Outline each Plasmodium falciparum-infected red blood cell.
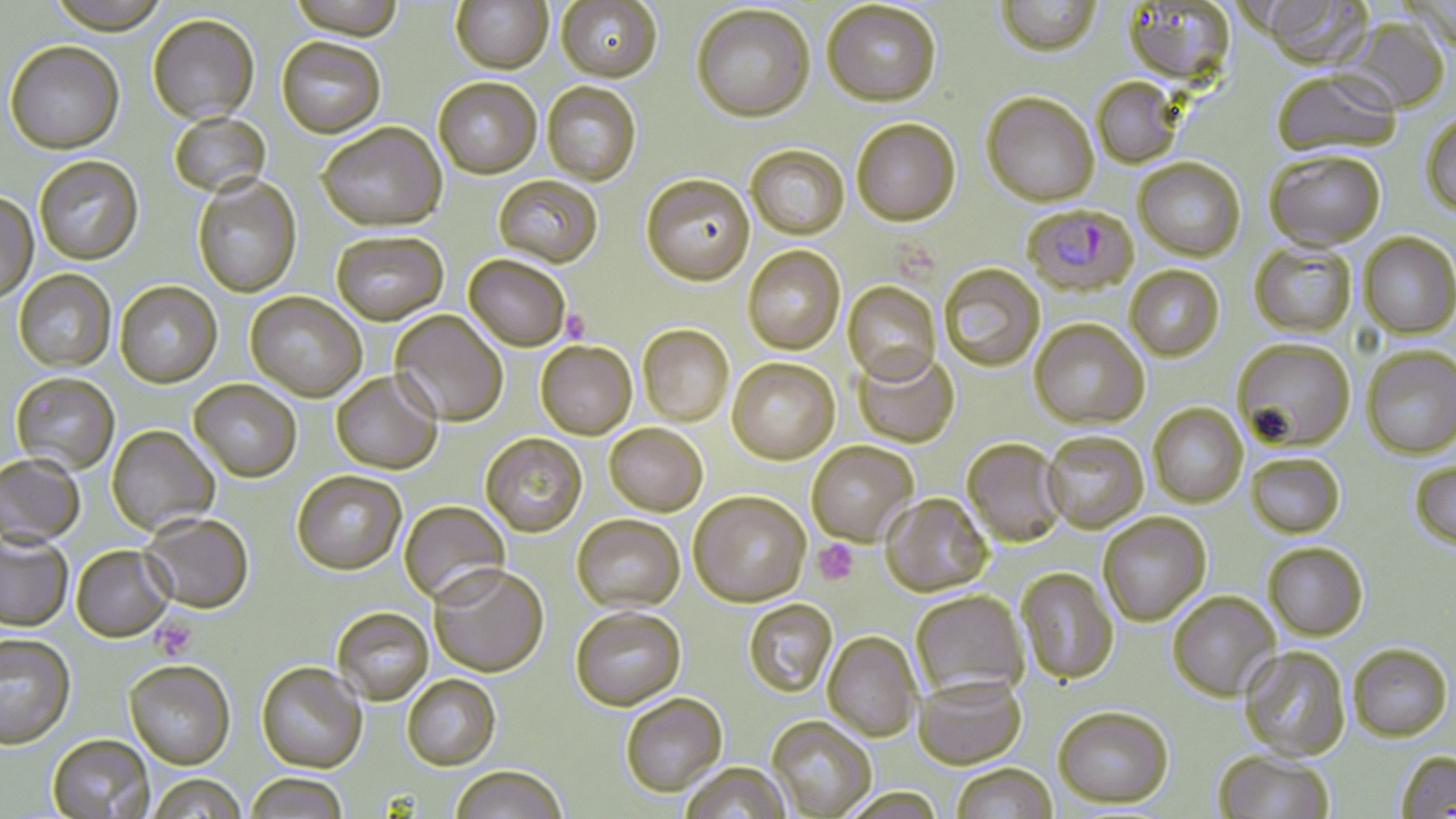

Approximate bounding boxes as named x1/y1/x2/y2 corners in pixels.
Plasmodium falciparum-infected red blood cells: (x1=1025, y1=207, x2=1141, y2=300).

{
  "slide_level_diagnosis": "Plasmodium falciparum",
  "modality": "optical microscopy",
  "field_of_view": "one of a larger specimen",
  "uninfected_red_blood_cell_locations": "approximate bounding boxes as named x1/y1/x2/y2 corners in pixels: (x1=47, y1=0, x2=170, y2=34), (x1=288, y1=0, x2=405, y2=40), (x1=450, y1=0, x2=553, y2=73), (x1=556, y1=0, x2=662, y2=82), (x1=995, y1=0, x2=1102, y2=57), (x1=1258, y1=0, x2=1373, y2=69), (x1=822, y1=1, x2=941, y2=107), (x1=1123, y1=2, x2=1237, y2=87), (x1=692, y1=5, x2=815, y2=123), (x1=148, y1=14, x2=259, y2=123), (x1=1337, y1=17, x2=1451, y2=115), (x1=277, y1=37, x2=386, y2=138), (x1=5, y1=41, x2=124, y2=153), (x1=1271, y1=71, x2=1401, y2=157), (x1=1091, y1=77, x2=1183, y2=170), (x1=433, y1=78, x2=541, y2=178), (x1=542, y1=82, x2=641, y2=185), (x1=981, y1=92, x2=1099, y2=206), (x1=169, y1=112, x2=271, y2=198), (x1=1421, y1=112, x2=1456, y2=219), (x1=851, y1=118, x2=961, y2=226), (x1=317, y1=122, x2=446, y2=231), (x1=746, y1=145, x2=850, y2=239), (x1=1264, y1=150, x2=1385, y2=249), (x1=34, y1=156, x2=143, y2=264), (x1=1133, y1=157, x2=1246, y2=261), (x1=641, y1=173, x2=755, y2=286), (x1=494, y1=175, x2=603, y2=268), (x1=193, y1=176, x2=302, y2=297), (x1=0, y1=192, x2=39, y2=303), (x1=332, y1=231, x2=448, y2=324), (x1=1359, y1=232, x2=1456, y2=339), (x1=1249, y1=242, x2=1356, y2=338), (x1=742, y1=245, x2=845, y2=354), (x1=464, y1=255, x2=571, y2=351), (x1=939, y1=264, x2=1045, y2=372), (x1=1124, y1=265, x2=1224, y2=361), (x1=14, y1=269, x2=116, y2=372), (x1=115, y1=281, x2=222, y2=387), (x1=843, y1=281, x2=941, y2=385), (x1=246, y1=291, x2=366, y2=401), (x1=390, y1=311, x2=509, y2=426), (x1=1029, y1=318, x2=1149, y2=429), (x1=637, y1=324, x2=734, y2=426), (x1=1232, y1=338, x2=1355, y2=451), (x1=536, y1=341, x2=637, y2=439), (x1=1362, y1=346, x2=1456, y2=459), (x1=853, y1=351, x2=960, y2=447), (x1=727, y1=358, x2=839, y2=464), (x1=332, y1=371, x2=443, y2=474), (x1=11, y1=372, x2=120, y2=474), (x1=190, y1=380, x2=302, y2=481), (x1=1148, y1=403, x2=1247, y2=507), (x1=605, y1=423, x2=708, y2=516), (x1=107, y1=425, x2=220, y2=535), (x1=1043, y1=431, x2=1148, y2=533), (x1=480, y1=433, x2=587, y2=536), (x1=961, y1=438, x2=1068, y2=547), (x1=806, y1=440, x2=919, y2=546), (x1=0, y1=453, x2=85, y2=547), (x1=1246, y1=453, x2=1345, y2=537), (x1=1409, y1=459, x2=1456, y2=548), (x1=292, y1=470, x2=407, y2=574), (x1=689, y1=491, x2=811, y2=606), (x1=881, y1=493, x2=992, y2=596), (x1=399, y1=500, x2=510, y2=606), (x1=141, y1=512, x2=254, y2=614), (x1=1099, y1=513, x2=1211, y2=625), (x1=572, y1=514, x2=684, y2=611), (x1=0, y1=531, x2=73, y2=632), (x1=1264, y1=542, x2=1368, y2=640), (x1=72, y1=545, x2=174, y2=641), (x1=429, y1=564, x2=548, y2=677), (x1=1016, y1=567, x2=1119, y2=685), (x1=911, y1=590, x2=1028, y2=699), (x1=1168, y1=591, x2=1280, y2=700), (x1=743, y1=599, x2=838, y2=697), (x1=570, y1=606, x2=686, y2=710), (x1=332, y1=607, x2=433, y2=704), (x1=823, y1=632, x2=921, y2=741), (x1=0, y1=634, x2=76, y2=748), (x1=1349, y1=644, x2=1452, y2=741), (x1=1239, y1=646, x2=1350, y2=760), (x1=124, y1=660, x2=236, y2=768), (x1=257, y1=661, x2=367, y2=773), (x1=402, y1=674, x2=500, y2=770), (x1=914, y1=675, x2=1026, y2=768), (x1=621, y1=693, x2=727, y2=796), (x1=1053, y1=706, x2=1174, y2=808), (x1=767, y1=716, x2=876, y2=818), (x1=47, y1=733, x2=155, y2=818), (x1=1213, y1=749, x2=1334, y2=818), (x1=1396, y1=750, x2=1456, y2=818), (x1=679, y1=762, x2=791, y2=819), (x1=951, y1=762, x2=1058, y2=819), (x1=450, y1=765, x2=567, y2=819), (x1=148, y1=774, x2=246, y2=819), (x1=245, y1=774, x2=347, y2=818)",
  "magnification": "1000x",
  "stain": "May-Grünwald-Giemsa",
  "preparation": "thin blood film",
  "image_size": "1456×819 pixels",
  "platelet_locations": "approximate bounding boxes as named x1/y1/x2/y2 corners in pixels: (x1=562, y1=309, x2=591, y2=343), (x1=813, y1=540, x2=859, y2=585), (x1=150, y1=615, x2=197, y2=659)"
}